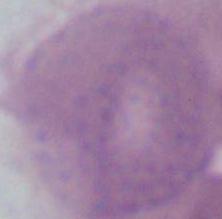
Captured at 1000x magnification. Micrograph. An erythrocyte is seen.